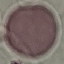
Summary:
  - Result: no malaria parasites detected
  - Capture: smartphone through the microscope eyepiece
  - Stain: Giemsa
  - Preparation: thin smear
  - Image type: cell patch, automatically extracted from a larger field of view and resized to 64 × 64 pixels